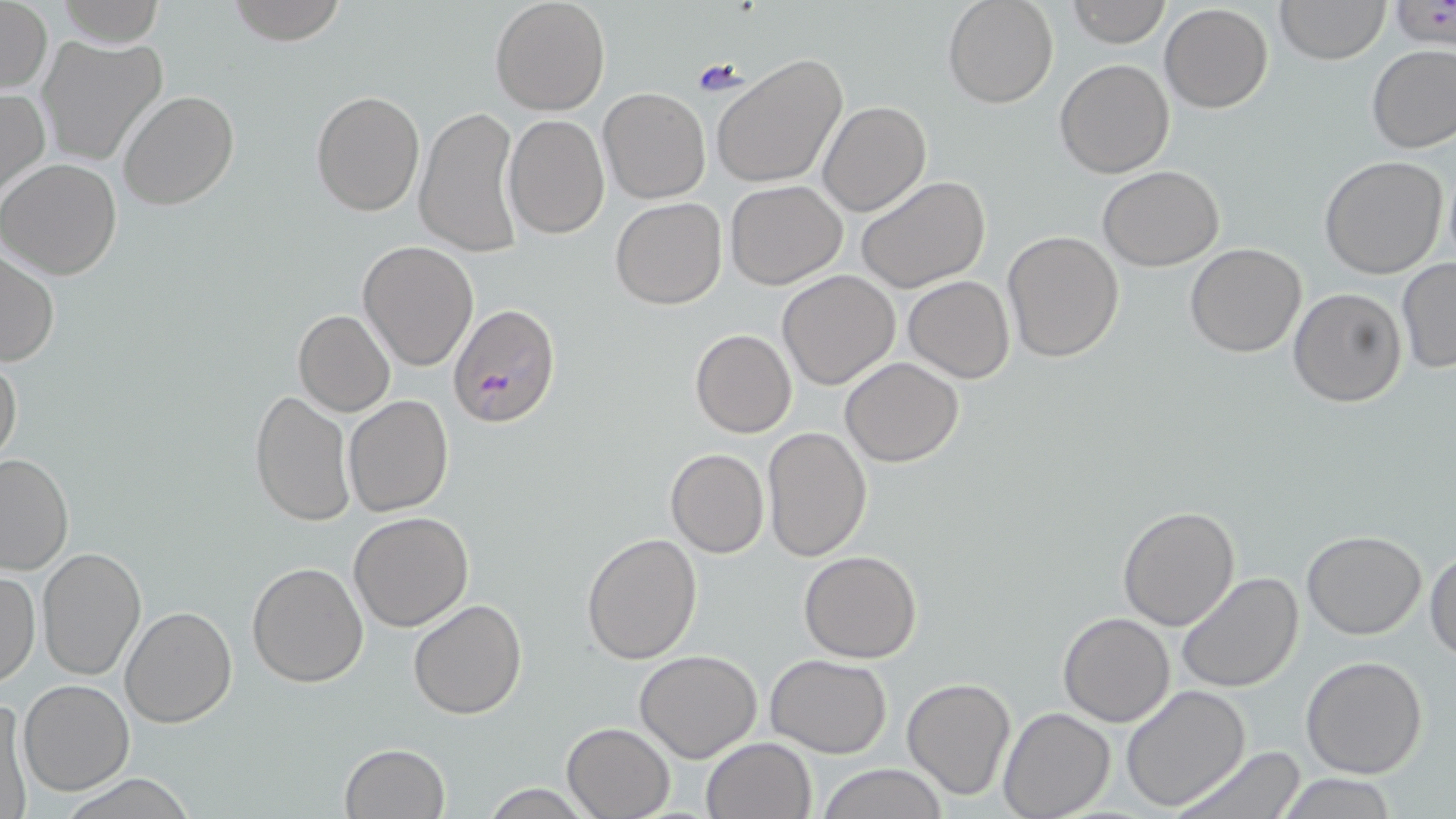
slide-level diagnosis = Plasmodium falciparum
stain = May-Grünwald-Giemsa
uninfected red blood cell locations = approximate bounding boxes as (x1,y1)-(x2,y2) corner pairs in pixels: (57,0)-(163,47), (224,0)-(347,44), (489,0)-(610,115), (942,0)-(1059,109), (1276,0)-(1388,64), (1389,0)-(1454,49), (1065,1)-(1170,48), (1,2)-(52,94), (1159,3)-(1273,114), (37,33)-(168,167), (1366,43)-(1456,154), (711,55)-(848,189), (1055,58)-(1175,178), (0,86)-(49,205), (597,87)-(711,205), (309,90)-(425,217), (117,91)-(238,211), (818,101)-(931,217), (413,104)-(524,257), (502,116)-(609,239), (1319,155)-(1450,280), (0,157)-(122,280), (1097,166)-(1223,271), (856,175)-(990,295), (725,180)-(848,290), (611,197)-(726,310), (1002,229)-(1125,362), (357,240)-(480,372), (1184,242)-(1306,357), (1,248)-(60,368), (1397,256)-(1456,375), (777,270)-(902,391), (903,275)-(1015,382), (1287,287)-(1406,407), (293,309)-(396,417), (689,329)-(797,439), (0,351)-(23,469), (841,358)-(964,468), (250,389)-(352,525), (343,394)-(454,517), (762,425)-(873,562), (664,448)-(769,558), (0,453)-(74,576), (1117,504)-(1240,631), (348,511)-(474,630), (1302,530)-(1427,640), (581,532)-(704,665), (36,547)-(148,682), (1425,548)-(1456,661), (799,549)-(922,663), (246,561)-(370,687), (0,568)-(40,689), (1176,571)-(1305,694), (408,598)-(528,720), (118,606)-(237,729), (1059,612)-(1175,727), (635,650)-(763,763), (767,654)-(892,758), (1301,655)-(1429,779), (900,677)-(1017,802), (18,679)-(134,797), (1121,683)-(1252,811), (1,694)-(32,816), (998,705)-(1114,819), (561,722)-(675,818), (701,737)-(817,819), (340,743)-(451,819), (1167,743)-(1311,819), (816,763)-(947,819), (60,774)-(200,817), (1279,775)-(1400,817), (478,783)-(595,818)
modality = optical microscopy
magnification = 1000x
preparation = thin blood smear
image size = 1456×819 pixels
Plasmodium falciparum-infected red blood cell locations = approximate bounding boxes as (x1,y1)-(x2,y2) corner pairs in pixels: (448,304)-(560,430)
field of view = one of a larger specimen